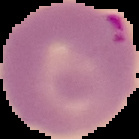 Image is 139×139 pixels. From a thin blood film. Result: malaria parasites detected. Cell region segmented out of the field of view; the surrounding area is masked to black.